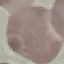
Summary:
  - Result: negative for malaria parasites
  - Preparation: thin smear
  - Image type: automatically extracted cell patch, resized to 64 × 64 pixels
  - Capture: smartphone camera at the microscope eyepiece
  - Stain: Giemsa